Comment on the morphology of the red blood cells.
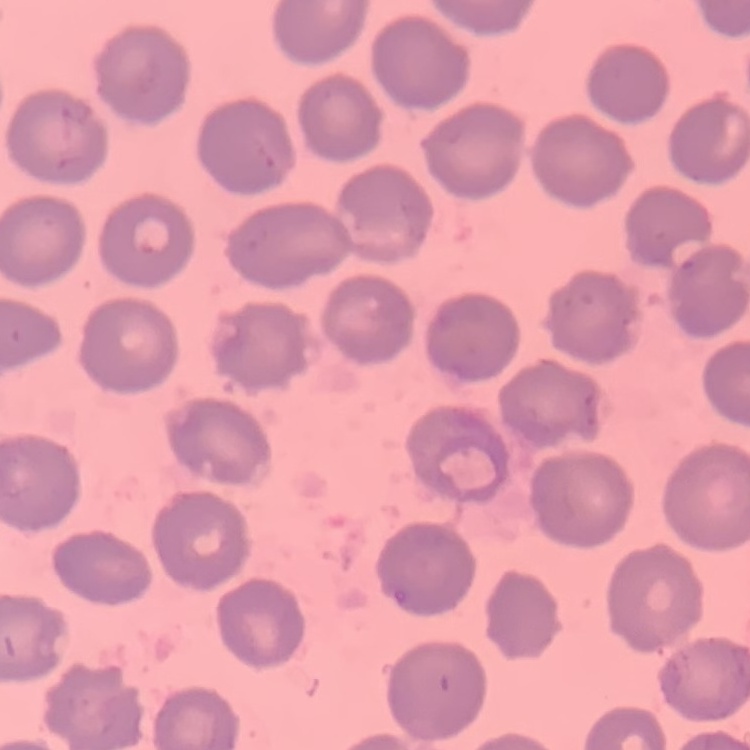

They show no rouleaux formation.

image_type: square crop of a larger photomicrograph
preparation: thin peripheral smear
stain: Field's or Giemsa